Classify this cell by malaria status.
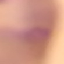
Uninfected.

image type = automatically extracted cell patch, resized to 64 × 64 pixels
preparation = thin blood smear
capture = smartphone through the microscope eyepiece
stain = Giemsa